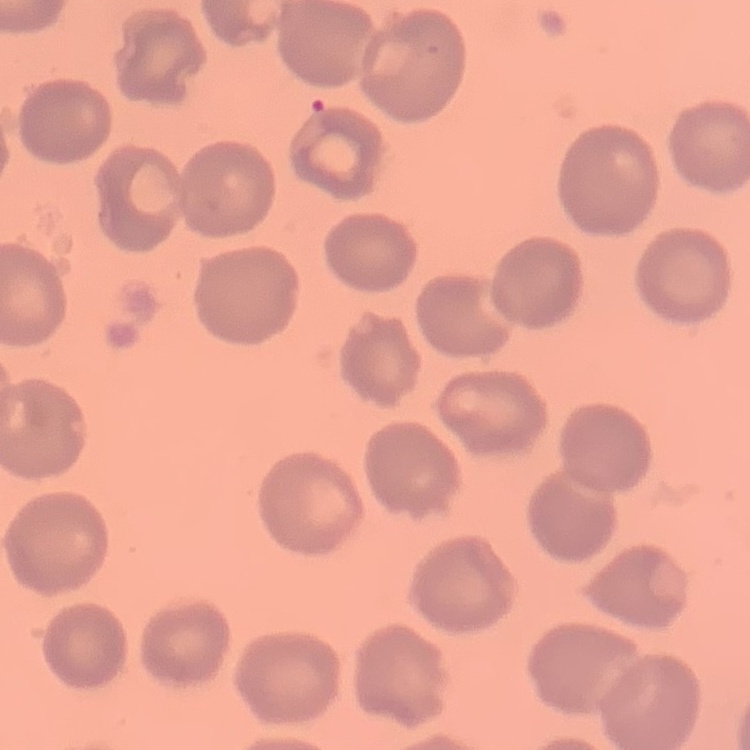

The erythrocytes show no rouleaux formation. Square crop of a larger photomicrograph. Thin blood film. Stained with either Field's or Giemsa.